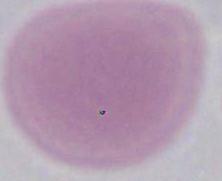
Summary:
  - Modality: micrograph
  - Identification: erythrocyte
  - Magnification: 1000x